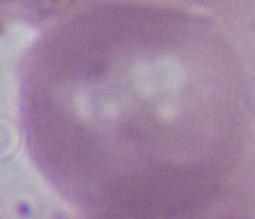
Summary:
  - Identification: erythrocyte
  - Modality: photomicrograph
  - Magnification: 1000x